Name the parasite shown.
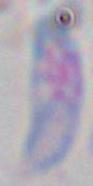
Toxoplasma gondii.

magnification = 1000x
modality = micrograph